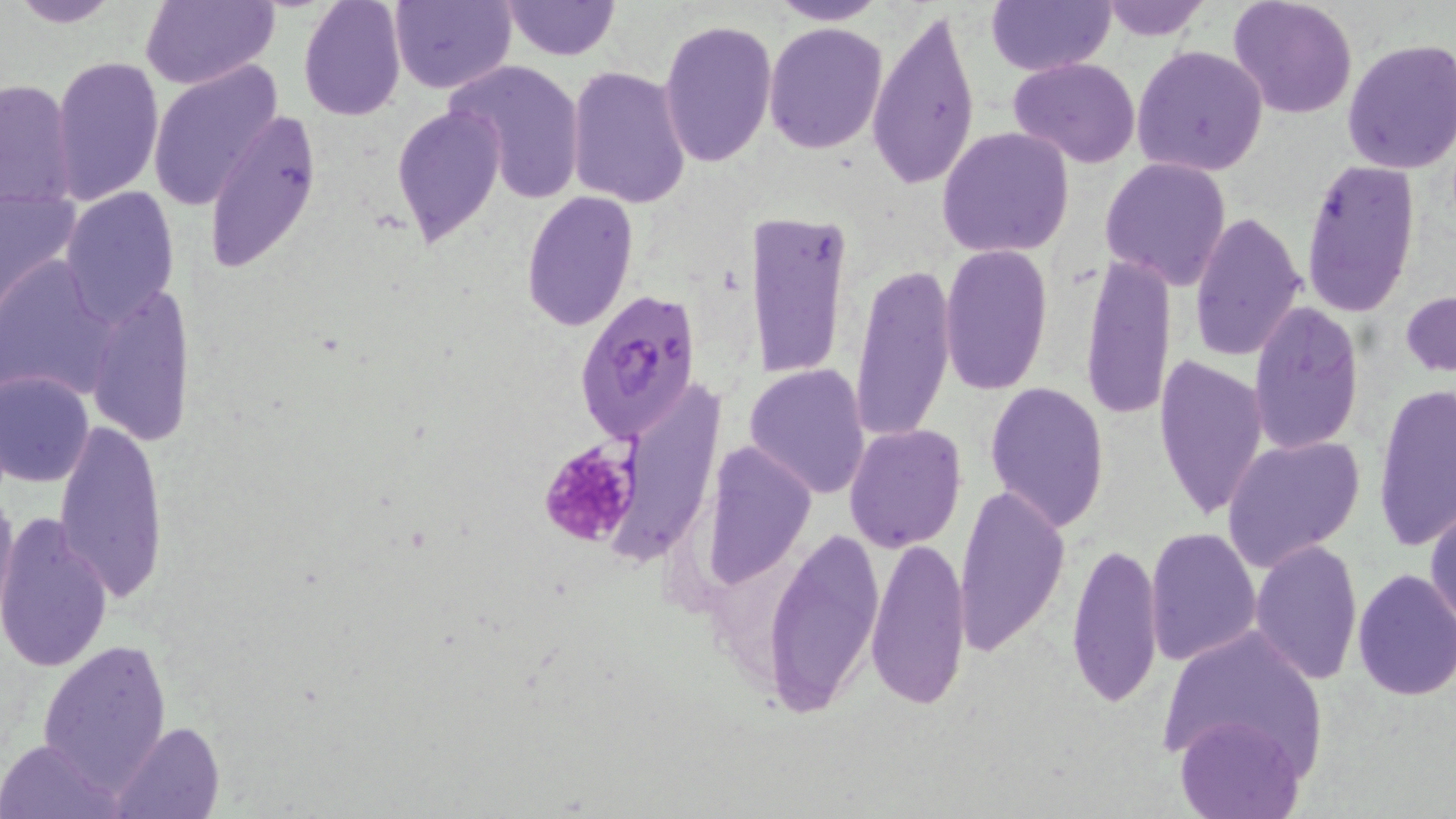
Summary:
  - Coordinate format: approximate bounding boxes as (x1, y1, x2, y2) in pixels
  - Uninfected red blood cell locations: (4, 0, 126, 29), (139, 0, 280, 90), (297, 0, 407, 120), (389, 0, 515, 93), (502, 0, 618, 60), (769, 0, 891, 25), (985, 0, 1116, 78), (1093, 0, 1212, 41), (1229, 0, 1357, 120), (867, 7, 981, 190), (658, 19, 776, 167), (764, 22, 887, 153), (1340, 38, 1456, 177), (1132, 45, 1269, 177), (50, 53, 161, 205), (1009, 57, 1140, 168), (445, 58, 586, 205), (147, 62, 284, 211), (566, 65, 692, 208), (1, 77, 78, 210), (390, 103, 504, 248), (202, 108, 322, 276), (937, 127, 1074, 258), (1100, 155, 1233, 290), (1300, 160, 1423, 317), (0, 187, 83, 310), (63, 187, 179, 321), (521, 190, 638, 332), (748, 210, 853, 380), (1188, 210, 1307, 363), (940, 244, 1053, 397), (1079, 252, 1175, 424), (0, 256, 119, 400), (849, 264, 956, 445), (84, 282, 196, 446), (1401, 291, 1455, 376), (1245, 302, 1365, 456), (1153, 351, 1268, 522), (744, 363, 871, 499), (0, 369, 95, 487), (1, 382, 131, 562), (984, 382, 1112, 531), (1373, 384, 1455, 552), (53, 418, 171, 606), (845, 423, 965, 552), (1224, 434, 1362, 568), (696, 441, 815, 597), (954, 484, 1071, 655), (0, 489, 19, 627), (1427, 499, 1456, 634), (1, 512, 114, 673), (768, 527, 883, 715), (1144, 527, 1262, 667), (866, 534, 971, 711), (1249, 539, 1362, 686), (1066, 540, 1163, 709), (1351, 567, 1456, 702), (1160, 623, 1329, 775), (37, 637, 172, 791), (1176, 714, 1305, 819), (115, 720, 223, 819), (0, 738, 122, 819)
  - Plasmodium falciparum-infected red blood cell locations: (573, 287, 704, 444)
  - Platelet locations: (539, 439, 641, 550)
  - Slide-level diagnosis: Plasmodium falciparum
  - Modality: light microscopy
  - Field of view: single
  - Magnification: 1000x
  - Image size: 1456×819 pixels
  - Stain: May-Grünwald-Giemsa
  - Preparation: thin blood film